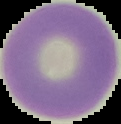

{
  "malaria_status": "uninfected",
  "image_size": "121×124 pixels",
  "preparation": "thin blood film",
  "image_type": "cell region segmented out of the field of view; surrounding area masked to black"
}